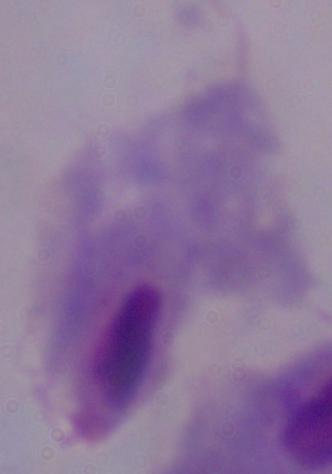
{
  "identification": "trichomonad",
  "modality": "photomicrograph",
  "magnification": "1000x"
}